Classify this cell by malaria status.
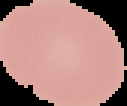
It is uninfected.

{
  "image_size": "127×106 pixels",
  "image_type": "cell region segmented out of the field of view; surrounding area masked to black",
  "preparation": "thin blood smear"
}